Locate platelets.
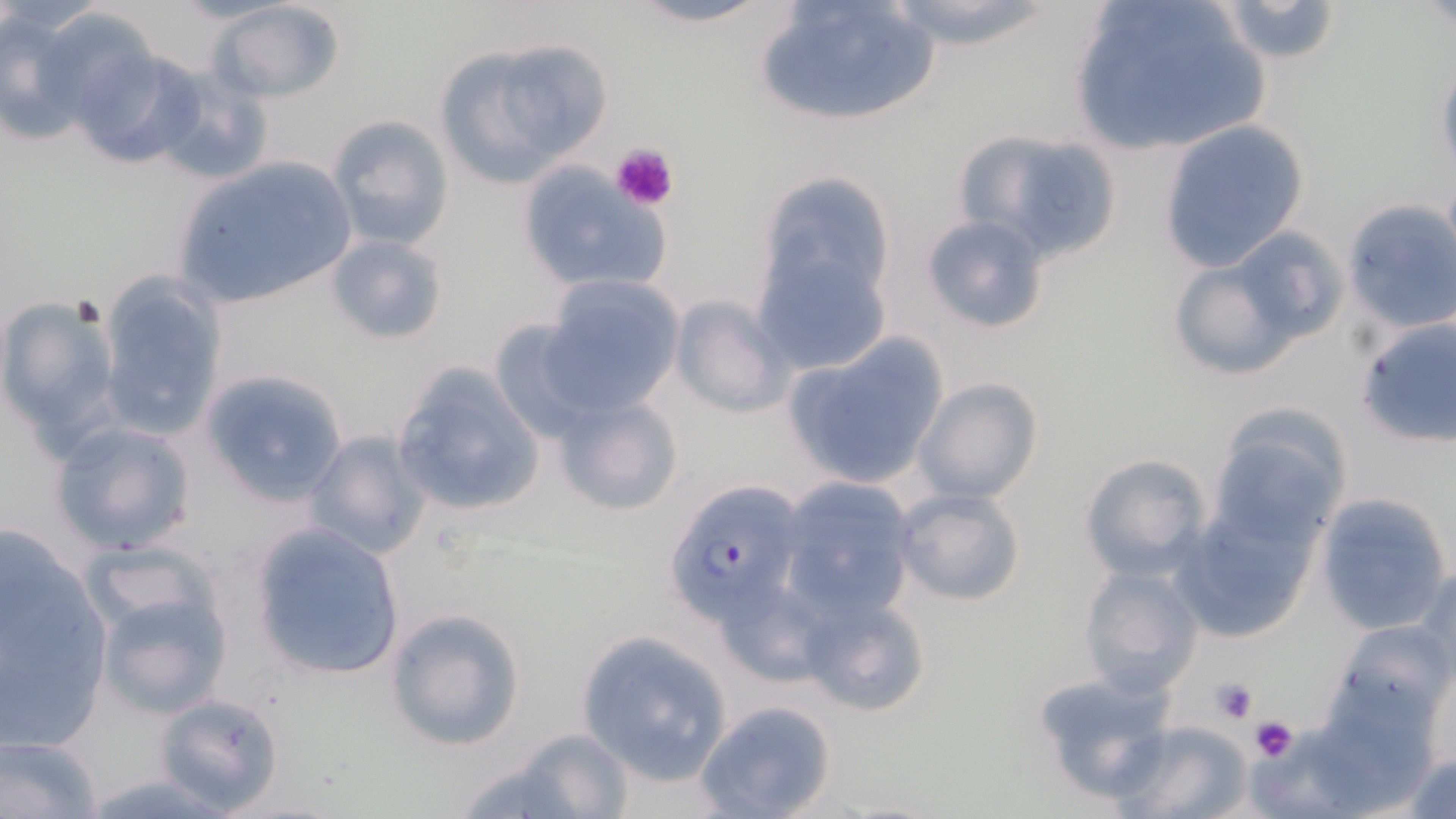

Approximate bounding boxes as (x1, y1, x2, y2) in pixels.
Platelets: (605, 141, 680, 213), (1208, 676, 1259, 724), (1249, 716, 1298, 763).

slide_level_diagnosis: Plasmodium falciparum
image_size: 1456×819 pixels
uninfected_red_blood_cell_locations: 'approximate bounding boxes as (x1, y1, x2, y2) in pixels: (210, 0, 348, 103), (619, 0, 786, 28), (751, 0, 942, 129), (876, 0, 1062, 49), (1068, 0, 1273, 156), (1212, 0, 1343, 64), (32, 5, 164, 130), (1, 8, 90, 146), (431, 34, 615, 188), (67, 45, 202, 172), (1434, 53, 1456, 183), (147, 69, 272, 186), (325, 114, 452, 251), (1158, 121, 1311, 271), (952, 129, 1126, 264), (166, 155, 360, 314), (513, 159, 672, 297), (1341, 200, 1456, 332), (752, 205, 898, 378), (919, 213, 1054, 335), (325, 234, 450, 346), (1165, 240, 1325, 383), (95, 272, 226, 439), (540, 274, 685, 414), (1, 294, 124, 442), (670, 296, 793, 418), (1356, 316, 1456, 451), (486, 318, 605, 445), (782, 339, 950, 490), (390, 360, 546, 519), (201, 368, 350, 506), (912, 378, 1043, 506), (553, 391, 686, 516), (1205, 404, 1355, 550), (50, 420, 198, 555), (302, 428, 432, 560), (1078, 453, 1215, 582), (774, 479, 918, 620), (891, 487, 1028, 608), (1314, 493, 1451, 634), (1173, 501, 1321, 641), (248, 520, 407, 681), (1, 541, 111, 750), (1077, 564, 1203, 696), (1413, 565, 1456, 688), (88, 579, 232, 718), (799, 594, 930, 718), (383, 606, 527, 752), (1327, 620, 1456, 735), (574, 631, 733, 783), (1417, 655, 1456, 775), (1032, 672, 1174, 806), (1303, 688, 1440, 815), (150, 692, 286, 814), (694, 698, 837, 819), (1113, 721, 1253, 819), (1244, 721, 1381, 818), (464, 731, 635, 818), (1, 733, 103, 818), (1400, 746, 1456, 819)'
preparation: thin blood film
stain: May-Grünwald-Giemsa
field_of_view: single
plasmodium_falciparum_infected_red_blood_cell_locations: 'approximate bounding boxes as (x1, y1, x2, y2) in pixels: (664, 481, 805, 623)'
magnification: 1000x
modality: light microscopy